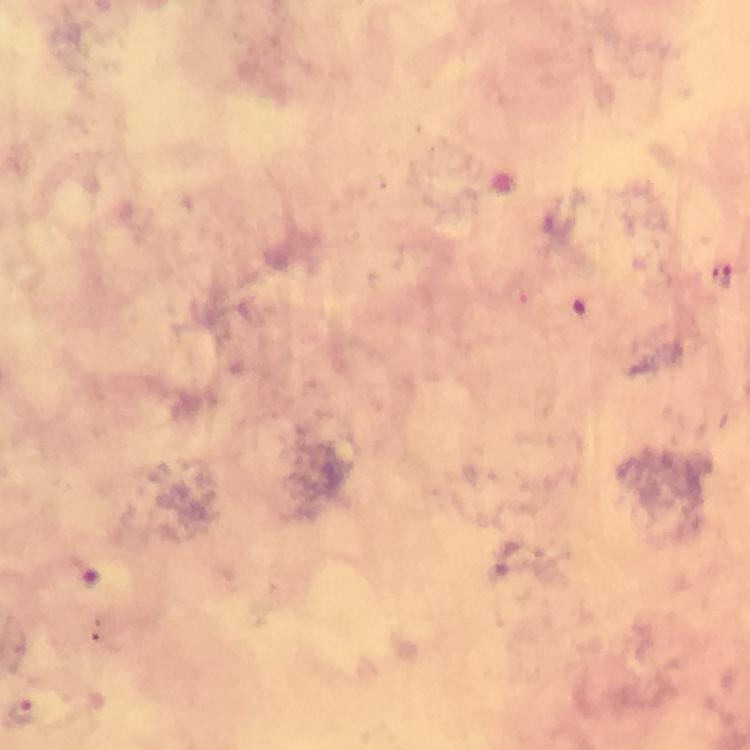

image size = 750×750 pixels
capture = smartphone photograph through a microscope
immersion oil = applied
cropped from = one field of view
context = from a malaria diagnostic workup
stain = Giemsa
preparation = thick blood smear
malaria parasite locations = approximate centers as (x, y) in pixels: (726, 276), (90, 575), (22, 710)
magnification = 100x